Comment on the morphology of the erythrocytes.
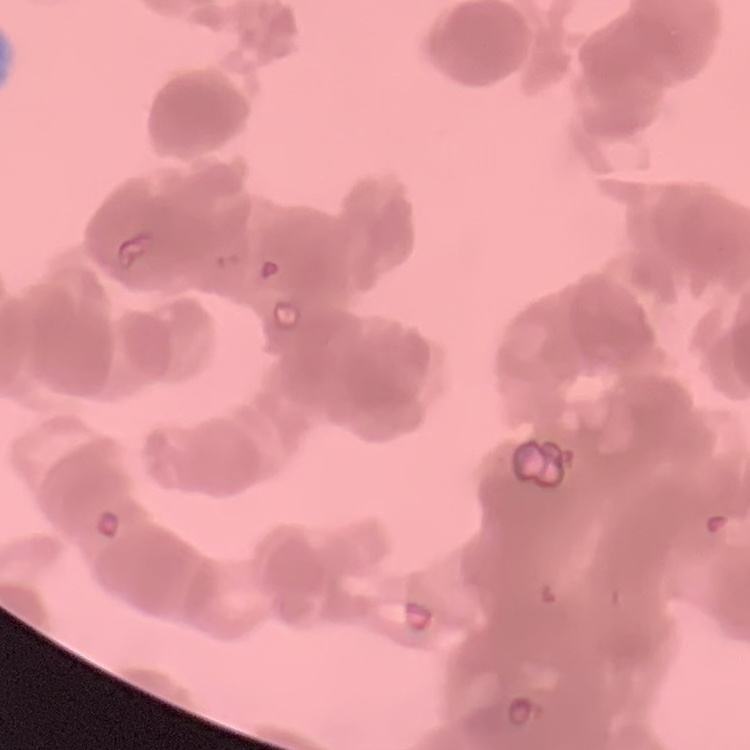
They show rouleaux formation.

preparation: thin peripheral smear
image_type: square crop of a larger photomicrograph
stain: Field's or Giemsa